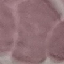

Result: no malaria parasites detected. Thin blood smear. Acquired by smartphone through the microscope eyepiece. Automatically extracted cell patch, resized to 64 × 64 pixels. Giemsa-stained preparation.